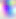

Summary:
  - Magnification: 400x
  - Identification: Toxoplasma gondii
  - Modality: micrograph